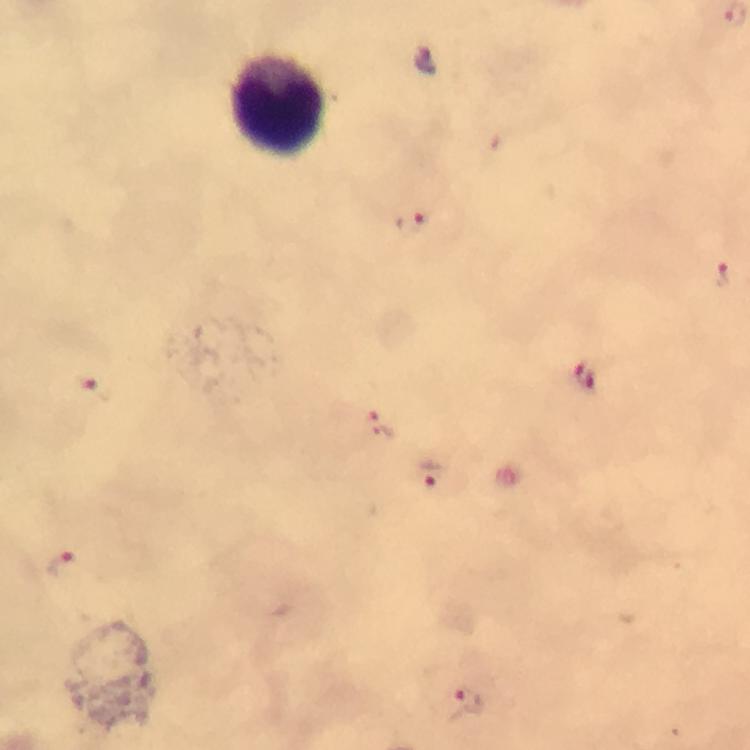
Approximate centers as (x, y) in pixels.
Summary:
  - Leukocyte locations: (279, 106)
  - Malaria parasite locations: (412, 223), (723, 274), (583, 376), (94, 389), (381, 426), (432, 474), (60, 565), (464, 701)
  - Capture: smartphone mounted on the microscope
  - Magnification: 100x
  - Stain: Giemsa
  - Context: from a malaria diagnostic workup
  - Cropped from: a single field of view
  - Immersion oil: used
  - Image size: 750×750 pixels
  - Preparation: thick blood smear